Report the malaria status of this cell.
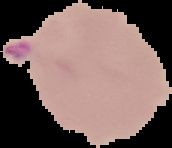
Parasitized.

Summary:
  - Preparation: thin blood film
  - Image size: 172×148 pixels
  - Image type: cell region segmented out of the field of view; surrounding area masked to black